Comment on the morphology of the red blood cells.
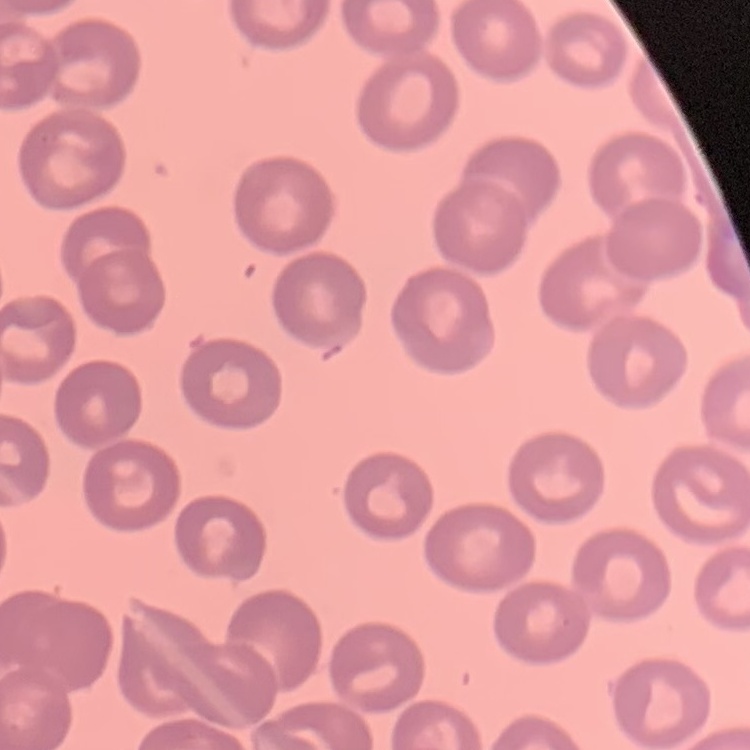
They show no rouleaux formation.

Square crop of a larger photomicrograph. Field's or Giemsa stain. Thin blood smear.